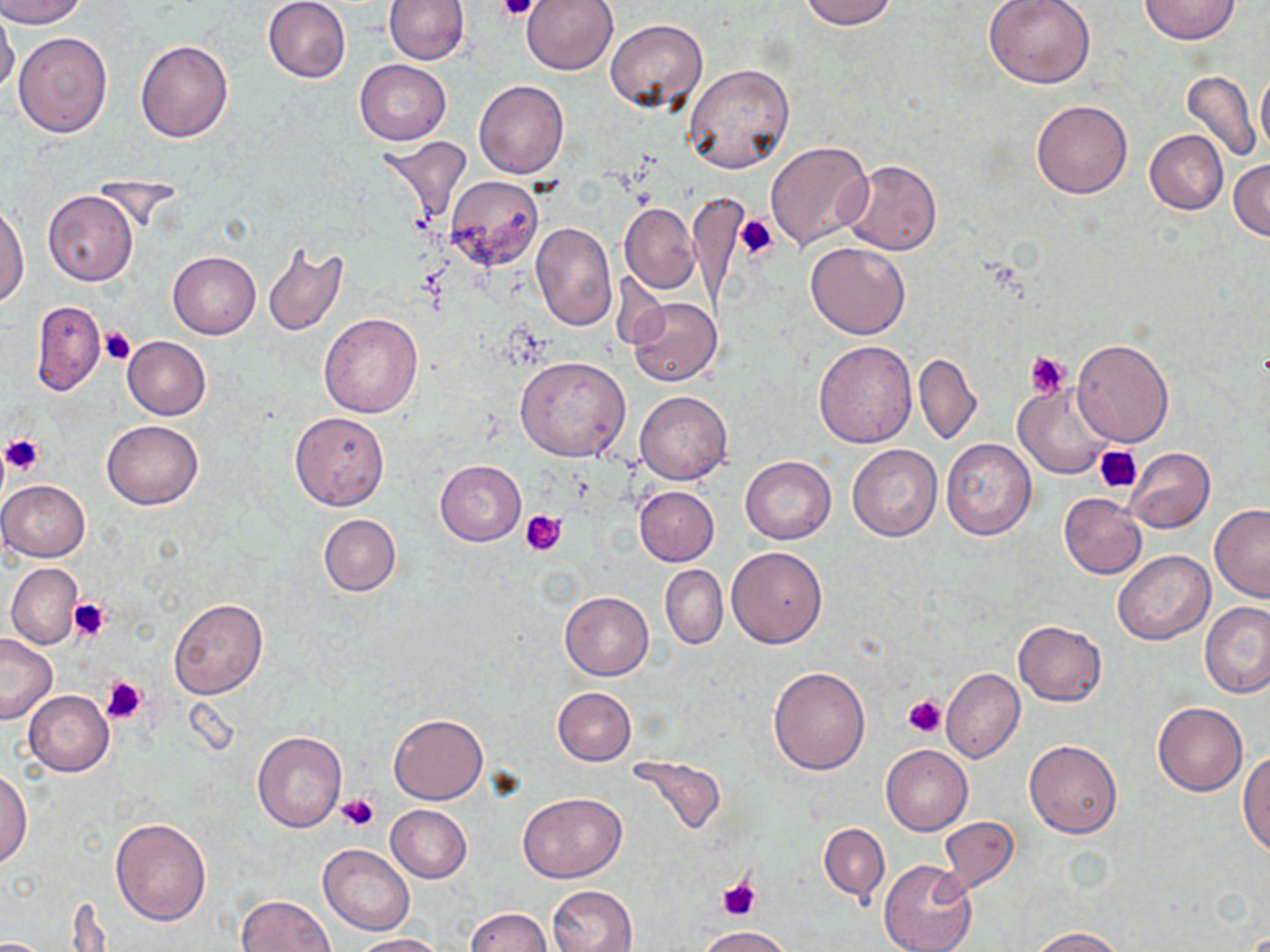

slide-level diagnosis = no evidence of blood parasites
preparation = thin blood smear
uninfected red blood cell locations = approximate bounding boxes as (x1, y1, x2, y2) in pixels: (0, 0, 87, 28), (262, 0, 352, 83), (384, 0, 470, 65), (519, 0, 618, 76), (798, 0, 899, 30), (985, 0, 1096, 88), (1139, 0, 1239, 44), (0, 5, 20, 95), (607, 19, 708, 112), (12, 31, 112, 138), (135, 40, 233, 143), (355, 59, 451, 144), (683, 65, 794, 175), (1181, 69, 1260, 163), (1255, 71, 1270, 155), (474, 80, 568, 179), (1032, 100, 1133, 199), (1145, 130, 1228, 214), (376, 135, 473, 229), (765, 141, 875, 251), (1229, 158, 1270, 241), (842, 160, 942, 256), (444, 176, 544, 269), (42, 190, 139, 286), (689, 192, 750, 307), (0, 203, 29, 309), (620, 203, 700, 294), (530, 221, 618, 332), (261, 241, 348, 337), (805, 241, 911, 339), (168, 251, 261, 339), (627, 295, 724, 386), (29, 302, 106, 394), (319, 312, 424, 419), (122, 336, 211, 420), (1072, 338, 1174, 447), (813, 341, 917, 446), (914, 353, 981, 446), (515, 356, 629, 462), (1014, 384, 1113, 480), (635, 391, 733, 484), (289, 411, 390, 510), (103, 421, 203, 509), (940, 438, 1036, 539), (847, 444, 942, 541), (1126, 447, 1215, 533), (740, 456, 836, 543), (435, 460, 526, 546), (0, 479, 90, 563), (634, 486, 719, 565), (1058, 493, 1146, 579), (1209, 503, 1270, 601), (319, 514, 401, 597), (726, 547, 827, 648), (1113, 550, 1215, 645), (5, 563, 82, 651), (660, 566, 727, 649), (559, 591, 653, 680), (167, 597, 267, 700), (1201, 601, 1270, 698), (1013, 621, 1106, 705), (0, 633, 57, 724), (768, 666, 870, 774), (941, 668, 1024, 762), (552, 686, 637, 765), (23, 690, 113, 777), (1153, 702, 1247, 796), (389, 713, 488, 804), (251, 732, 346, 832), (1024, 740, 1122, 838), (881, 744, 973, 834), (1239, 750, 1270, 855), (626, 754, 728, 837), (0, 768, 32, 868), (518, 792, 626, 883), (386, 805, 471, 883), (110, 817, 212, 925), (938, 817, 1020, 893), (819, 823, 889, 903), (318, 844, 415, 935), (879, 859, 977, 952), (547, 884, 636, 952), (237, 893, 336, 952), (465, 908, 551, 951), (695, 926, 792, 951), (1028, 926, 1124, 951), (351, 933, 447, 952)
image size = 1270×952 pixels
magnification = 1000x
field of view = one of a larger specimen
modality = optical microscopy
platelet locations = approximate bounding boxes as (x1, y1, x2, y2) in pixels: (499, 0, 537, 22), (735, 214, 777, 258), (99, 326, 136, 364), (1026, 352, 1071, 397), (1, 432, 46, 475), (1094, 443, 1142, 493), (520, 510, 565, 557), (67, 598, 111, 641), (101, 675, 147, 723), (902, 696, 944, 737), (336, 793, 380, 832), (718, 877, 759, 921)
stain = May-Grünwald-Giemsa